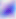
{
  "magnification": "400x",
  "modality": "photomicrograph",
  "identification": "Toxoplasma gondii"
}